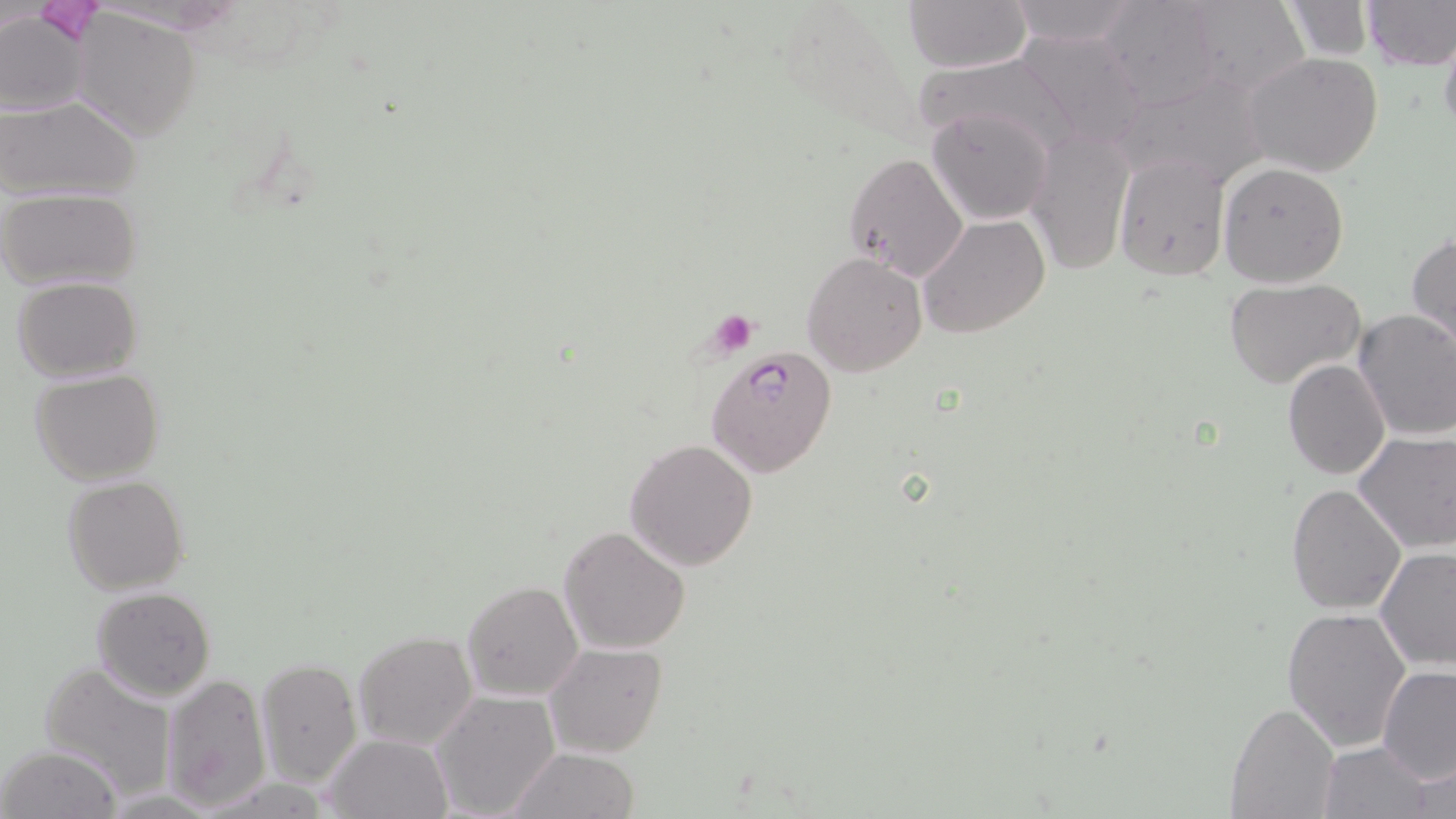

Summary:
  - Coordinate format: approximate bounding boxes as (x1,y1)-(x2,y2) corner pairs in pixels
  - Plasmodium falciparum-infected red blood cell locations: (705,348)-(837,480)
  - Uninfected red blood cell locations: (903,0)-(1033,71), (1005,0)-(1141,48), (1095,0)-(1229,109), (1176,0)-(1311,99), (1280,0)-(1374,60), (1360,0)-(1455,69), (0,10)-(92,116), (71,11)-(201,141), (1438,30)-(1456,150), (1015,31)-(1152,149), (1244,52)-(1384,176), (920,53)-(1085,161), (0,97)-(143,202), (925,106)-(1054,225), (1026,125)-(1136,272), (843,151)-(968,285), (1113,154)-(1229,279), (1218,160)-(1350,286), (0,187)-(143,290), (918,214)-(1050,340), (1407,232)-(1456,352), (802,252)-(928,376), (11,277)-(143,383), (1223,278)-(1366,390), (1353,309)-(1456,441), (1282,359)-(1391,479), (30,368)-(164,485), (1352,432)-(1456,554), (625,438)-(758,572), (62,475)-(190,596), (1285,482)-(1406,615), (558,525)-(691,654), (1375,546)-(1455,672), (460,579)-(583,703), (91,586)-(217,701), (1281,605)-(1413,752), (352,631)-(477,753), (546,643)-(668,758), (257,657)-(362,791), (38,660)-(177,798), (1378,664)-(1456,782), (160,673)-(273,810), (431,690)-(559,818), (1228,702)-(1338,818), (320,732)-(450,818), (1315,739)-(1437,819), (2,744)-(120,819), (508,747)-(638,819), (1399,748)-(1456,817)
  - Platelet locations: (33,2)-(107,44), (709,310)-(758,354)
  - Slide-level diagnosis: Plasmodium falciparum
  - Image size: 1456×819 pixels
  - Field of view: one of a larger specimen
  - Preparation: thin blood smear
  - Stain: May-Grünwald-Giemsa
  - Magnification: 1000x
  - Modality: light microscopy